Identify the parasite.
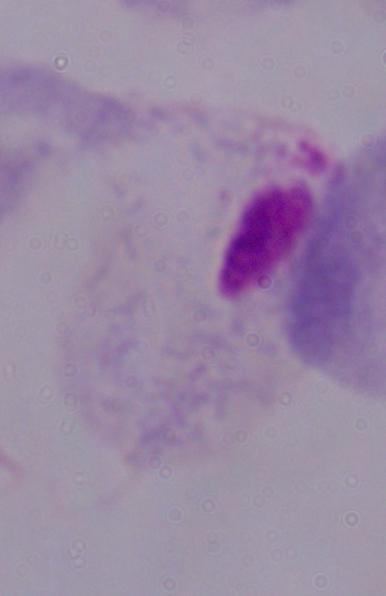

This is a trichomonad.

1000x magnification. Photomicrograph.